Assess this cell for malaria.
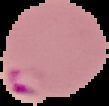

Parasitized.

Summary:
  - Image type: cell region segmented out of the field of view; surrounding area masked to black
  - Preparation: thin blood smear
  - Image size: 109×106 pixels